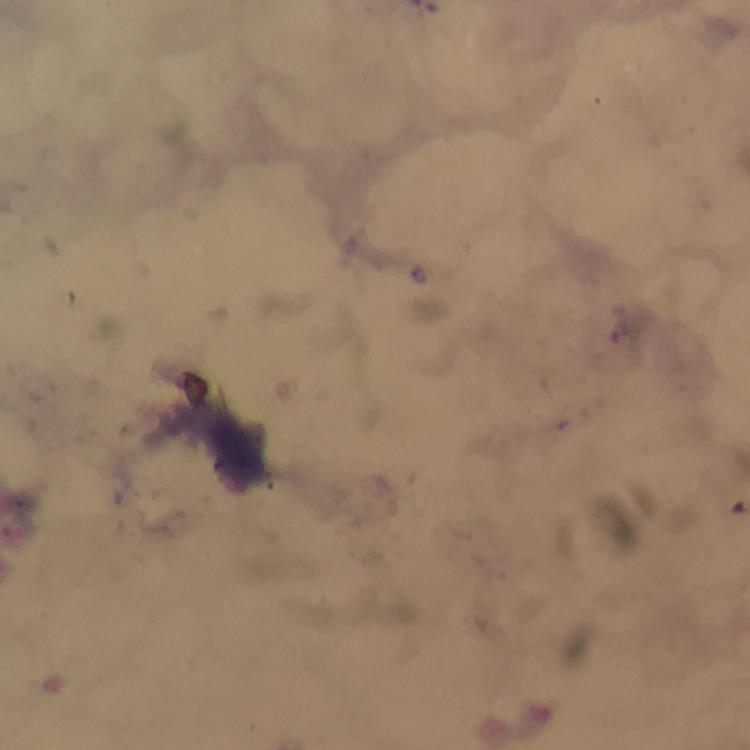

{
  "malaria_parasite_locations": "approximate object centers, in pixels from the top-left corner: (x=625, y=325)",
  "preparation": "thick smear",
  "context": "from a diagnostic examination for malaria",
  "magnification": "100x",
  "cropped_from": "a single field of view",
  "stain": "Giemsa",
  "immersion_oil": "applied",
  "capture": "smartphone photograph through a microscope",
  "image_size": "750×750 pixels"
}